Classify this cell by malaria status.
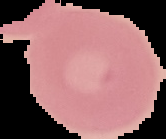

It is uninfected.

Summary:
  - Image type: segmented cell region on a black background
  - Image size: 166×139 pixels
  - Preparation: thin blood smear